Report the malaria status of this cell.
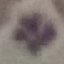

Uninfected.

image_type: cell patch, automatically extracted from a larger field of view and resized to 64 × 64 pixels
preparation: thin smear
capture: smartphone through the microscope eyepiece
stain: Giemsa